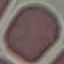
Summary:
  - Result: no malaria parasites detected
  - Stain: Giemsa
  - Capture: smartphone camera at the microscope eyepiece
  - Preparation: thin blood smear
  - Image type: automatically extracted cell patch, resized to 64 × 64 pixels